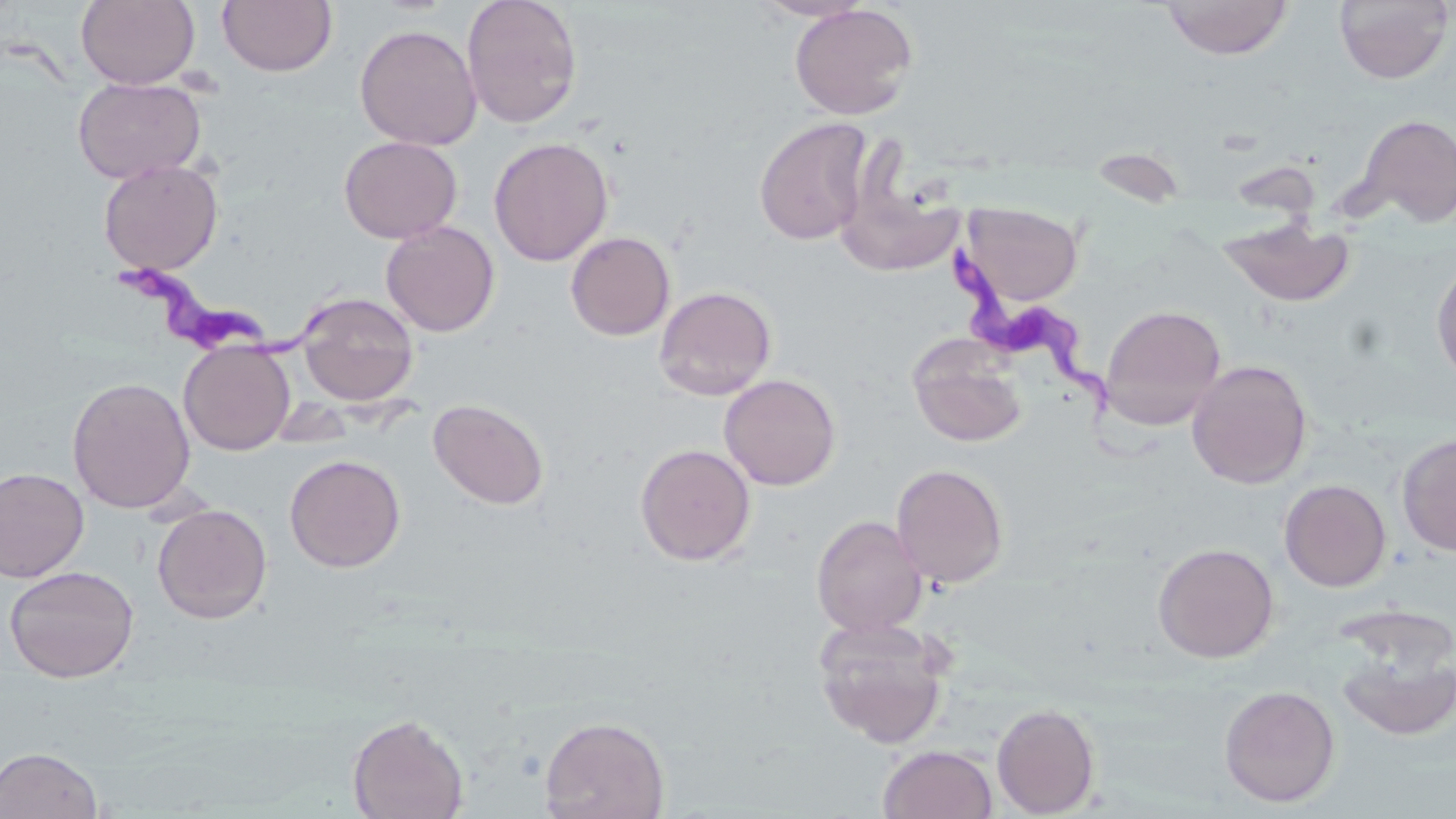

Approximate bounding boxes as (x1, y1, x2, y2) in pixels. Uninfected red blood cell locations: (77, 0, 199, 89), (217, 0, 337, 77), (460, 0, 583, 129), (752, 0, 871, 21), (1159, 0, 1293, 59), (1334, 0, 1453, 84), (790, 3, 918, 120), (354, 23, 482, 151), (73, 76, 205, 184), (1353, 113, 1456, 229), (754, 116, 874, 245), (338, 135, 462, 243), (489, 137, 613, 266), (98, 158, 223, 275), (837, 188, 966, 277), (962, 202, 1083, 306), (1216, 215, 1356, 308), (381, 221, 500, 337), (565, 231, 675, 341), (1432, 258, 1456, 388), (653, 285, 777, 401), (297, 292, 419, 407), (1100, 304, 1227, 429), (908, 337, 1028, 449), (179, 341, 295, 455), (1187, 359, 1312, 489), (719, 373, 841, 491), (67, 376, 195, 513), (428, 398, 549, 510), (1396, 432, 1456, 557), (635, 443, 756, 566), (284, 454, 406, 572), (891, 463, 1009, 588), (0, 467, 89, 582), (1279, 479, 1391, 592), (152, 503, 272, 624), (811, 515, 928, 636), (1153, 542, 1279, 663), (4, 564, 139, 683), (812, 615, 951, 748), (1336, 638, 1456, 743), (1219, 684, 1341, 807), (991, 702, 1100, 817), (346, 713, 469, 819), (540, 715, 670, 819), (878, 745, 997, 819), (0, 746, 104, 818). Trypanosoma brucei locations: (952, 250, 1152, 463), (113, 251, 343, 364). Slide-level diagnosis: Trypanosoma brucei. May-Grünwald-Giemsa stain. Captured at 1000x magnification. Image is 1456×819 pixels. Single field of view. Thin blood smear. Light microscopy.